Report the malaria status of this cell.
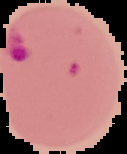

Parasitized.

Summary:
  - Preparation: thin blood film
  - Image type: cell region segmented out of the field of view; surrounding area masked to black
  - Image size: 127×154 pixels